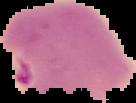
Summary:
  - Result: Plasmodium parasites identified
  - Image type: segmented cell region with the area outside set to black
  - Preparation: thin blood smear
  - Image size: 136×103 pixels